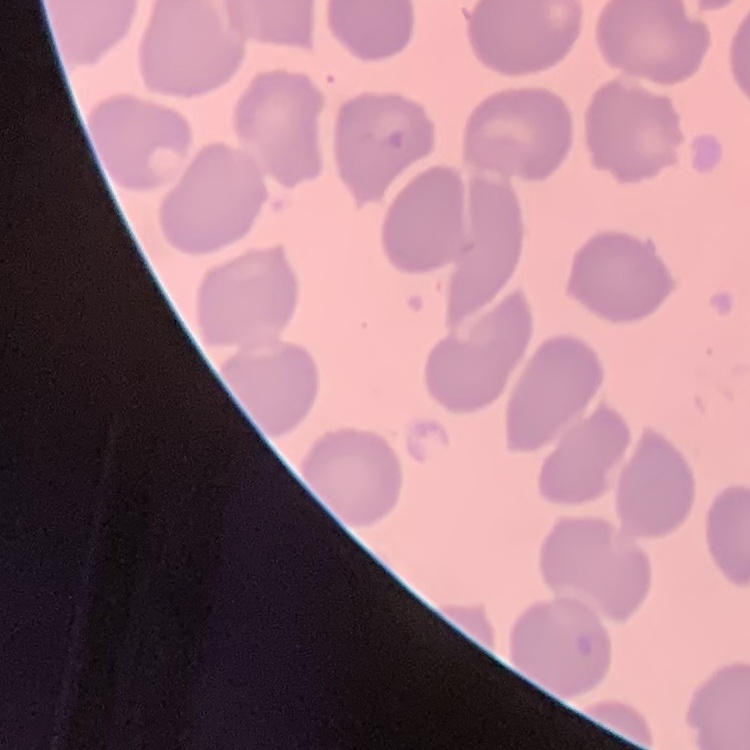 The red blood cells show no rouleaux formation. Stained with either Field's or Giemsa. Square crop of a larger photomicrograph. Thin blood smear.